Identify the preparation type.
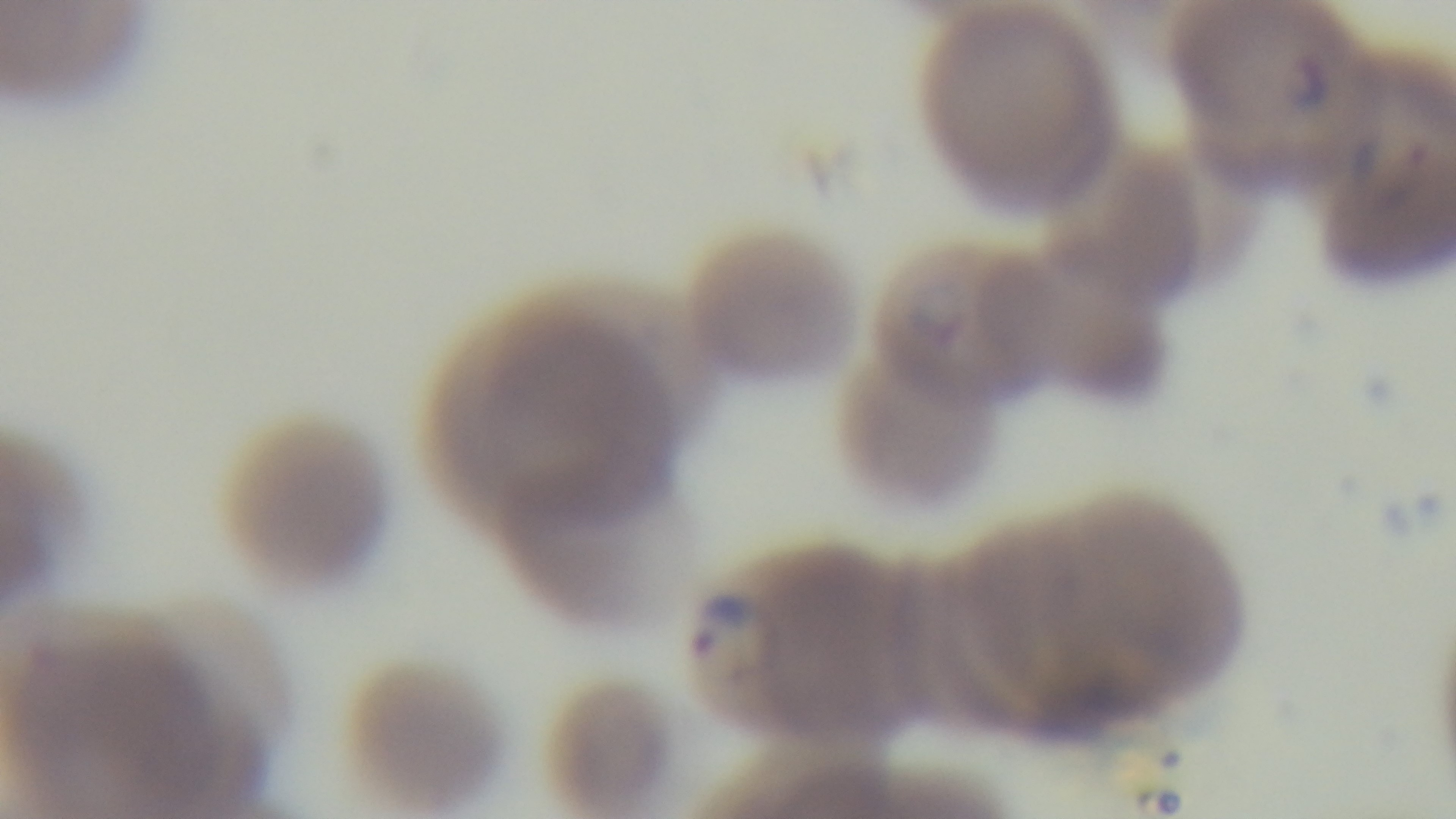

It is a thin blood film.

stain = Giemsa
malaria status = infected
modality = light microscopy
field of view = single
objective = 100x oil immersion
capture = mounted 4K digital camera